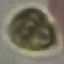

Malaria status: uninfected. Thin smear of blood. Giemsa-stained preparation. Photographed with a smartphone camera at the microscope eyepiece. Automatically extracted cell patch, resized to 64 × 64 pixels.